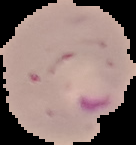

Result: malaria parasites detected. Image is 136×145 pixels. From a thin blood film. The area outside the segmented cell region is set to black.